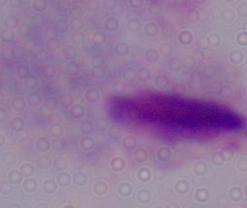
A trichomonad is seen. Photomicrograph. Captured at 1000x magnification.